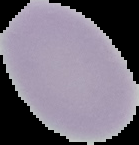
Cell region segmented out of the field of view; the surrounding area is masked to black. Image is 139×145 pixels. From a thin blood smear. Result: no Plasmodium parasites seen.